Evaluate for malaria.
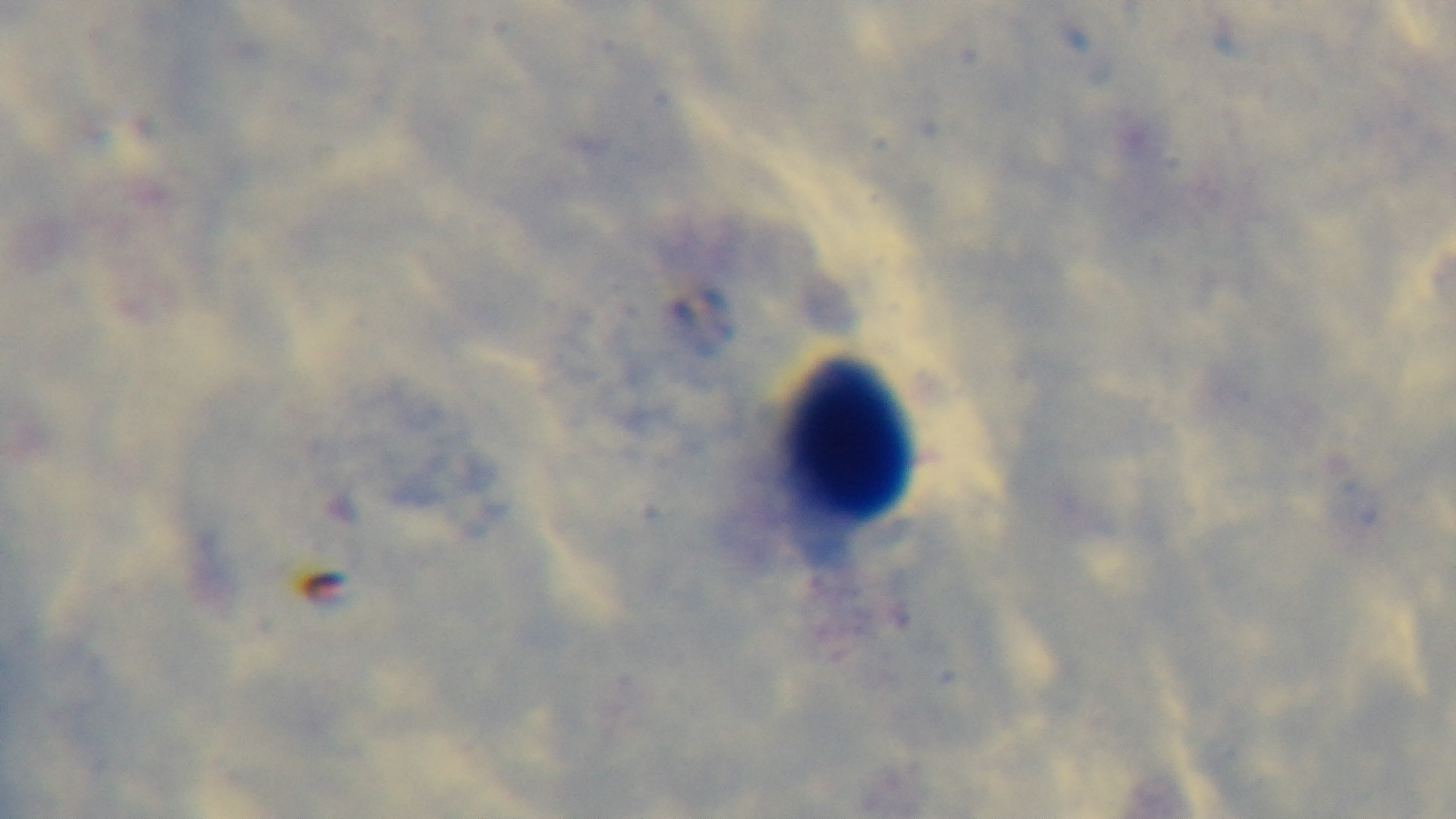

Uninfected.

Light microscopy. Giemsa-stained. Oil-immersion objective, 100x. Mounted 4K digital camera. Single field of view. Preparation: thick blood film.